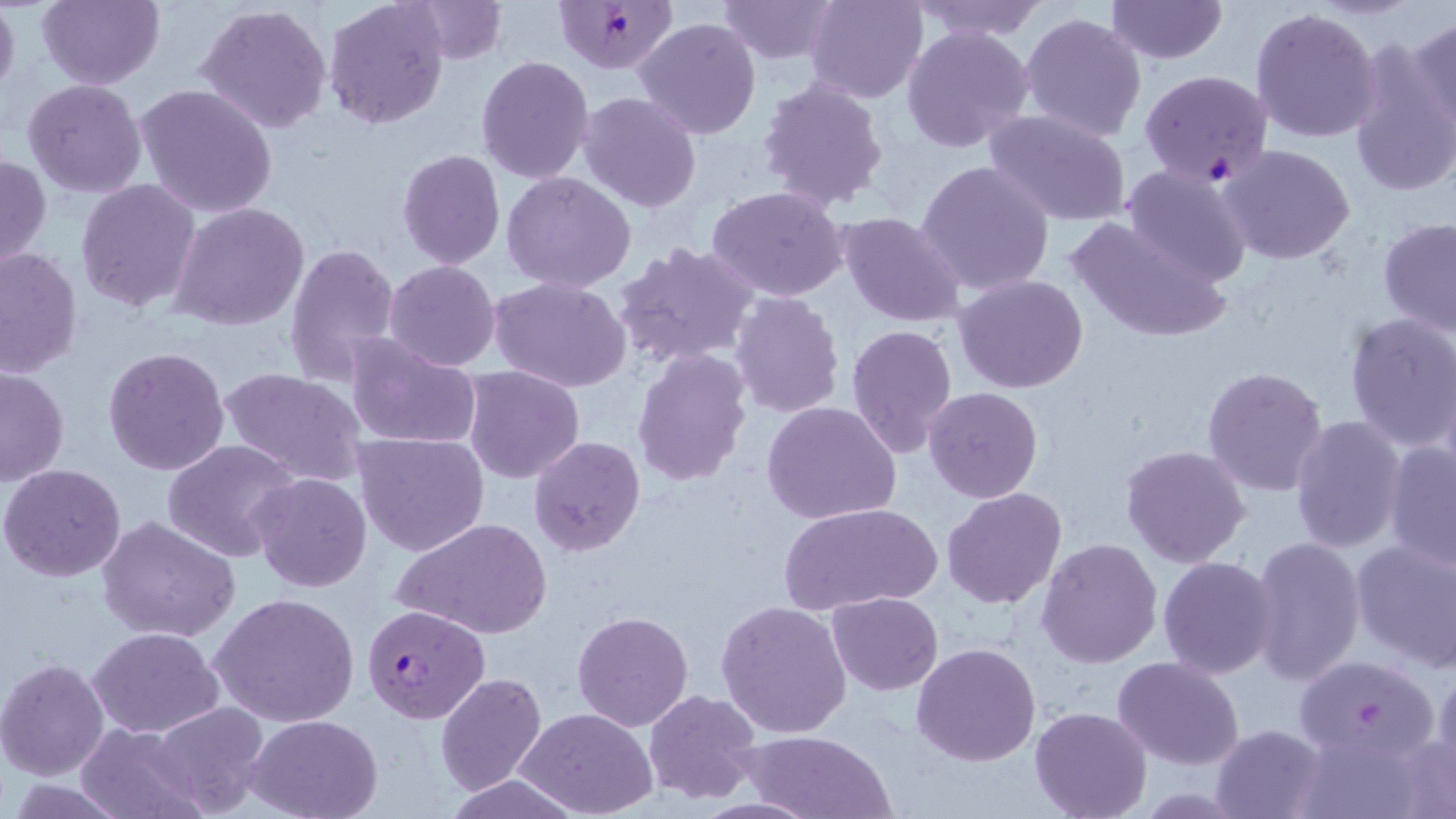

Summary:
  - Coordinate format: approximate bounding boxes as [x1, y1, x2, y2] in pixels
  - Uninfected red blood cell locations: [0, 0, 20, 102], [35, 0, 164, 89], [322, 0, 450, 131], [406, 0, 507, 65], [716, 0, 840, 64], [804, 0, 928, 104], [909, 0, 1049, 42], [1106, 0, 1227, 65], [195, 4, 334, 135], [1249, 6, 1384, 144], [1019, 11, 1147, 143], [1410, 15, 1456, 138], [634, 17, 762, 138], [902, 23, 1036, 154], [1347, 38, 1455, 199], [476, 55, 596, 185], [758, 76, 890, 212], [22, 79, 147, 199], [134, 84, 278, 219], [577, 91, 703, 213], [983, 108, 1133, 227], [1218, 143, 1356, 265], [396, 149, 505, 270], [0, 151, 49, 276], [914, 159, 1054, 297], [1119, 164, 1254, 287], [501, 171, 636, 294], [75, 178, 202, 312], [705, 186, 849, 301], [169, 201, 309, 330], [836, 211, 966, 327], [1068, 216, 1235, 346], [1378, 217, 1456, 335], [614, 241, 760, 368], [284, 242, 400, 386], [0, 246, 82, 380], [384, 260, 500, 370], [953, 272, 1088, 394], [488, 276, 632, 393], [730, 292, 845, 420], [1341, 312, 1456, 452], [845, 323, 959, 458], [342, 331, 481, 450], [103, 347, 230, 475], [631, 348, 751, 488], [218, 365, 368, 488], [0, 366, 69, 487], [463, 366, 584, 483], [1201, 367, 1330, 497], [923, 386, 1043, 503], [761, 400, 901, 524], [1288, 415, 1406, 557], [353, 431, 490, 557], [528, 436, 646, 555], [162, 440, 300, 563], [1383, 441, 1456, 571], [1122, 443, 1252, 568], [2, 464, 127, 583], [249, 472, 373, 593], [942, 487, 1068, 609], [779, 502, 942, 615], [98, 516, 241, 643], [392, 516, 554, 639], [1246, 534, 1367, 686], [1350, 536, 1456, 670], [1037, 537, 1162, 667], [1158, 556, 1279, 680], [209, 591, 360, 729], [826, 592, 943, 695], [718, 600, 852, 739], [572, 609, 692, 731], [87, 626, 224, 737], [911, 643, 1041, 767], [1290, 653, 1441, 769], [1113, 656, 1244, 770], [0, 658, 110, 781], [1426, 668, 1456, 792], [434, 672, 547, 795], [643, 688, 761, 803], [150, 702, 271, 816], [517, 707, 658, 817], [1028, 707, 1152, 819], [247, 715, 383, 819], [75, 722, 208, 819], [1210, 724, 1327, 818], [740, 729, 897, 818], [1289, 730, 1440, 819], [441, 774, 589, 819]
  - Plasmodium falciparum-infected red blood cell locations: [554, 0, 681, 76], [1139, 68, 1273, 188], [363, 603, 490, 723]
  - Slide-level diagnosis: Plasmodium falciparum
  - Modality: light microscopy
  - Stain: May-Grünwald-Giemsa
  - Field of view: single
  - Preparation: thin blood smear
  - Magnification: 1000x
  - Image size: 1456×819 pixels